State the blood parasite species.
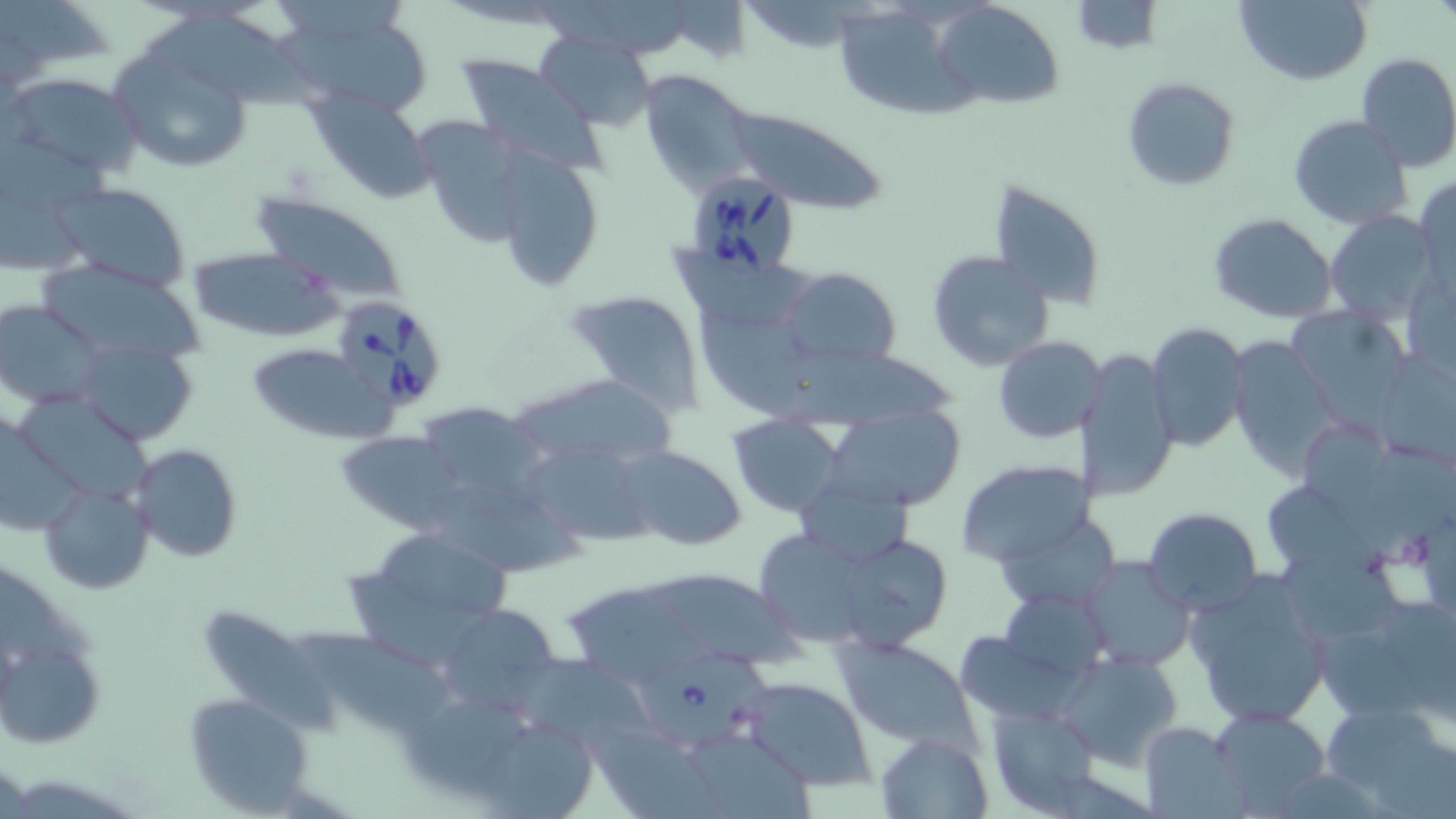
Babesia divergens.

Summary:
  - Coordinate format: approximate bounding boxes as [x1, y1, x2, y2] in pixels
  - Babesia divergens-infected red blood cell locations: [674, 169, 802, 288], [330, 294, 448, 412], [639, 649, 776, 752]
  - Uninfected red blood cell locations: [668, 0, 752, 62], [1069, 0, 1163, 53], [1235, 0, 1371, 86], [0, 2, 116, 88], [936, 2, 1061, 108], [277, 6, 430, 118], [144, 12, 326, 111], [827, 15, 990, 126], [536, 33, 655, 127], [106, 41, 256, 175], [1355, 51, 1456, 171], [455, 56, 605, 171], [641, 70, 762, 198], [6, 71, 146, 178], [1122, 76, 1241, 192], [310, 94, 436, 202], [715, 104, 886, 216], [1287, 114, 1413, 231], [418, 119, 532, 250], [494, 151, 606, 293], [1415, 176, 1456, 296], [986, 179, 1106, 310], [52, 181, 194, 292], [252, 194, 410, 304], [1326, 211, 1441, 325], [1209, 214, 1339, 324], [188, 247, 342, 342], [926, 250, 1054, 371], [672, 253, 835, 329], [37, 259, 205, 366], [779, 267, 901, 370], [565, 290, 705, 410], [0, 300, 105, 407], [1288, 309, 1412, 422], [1144, 323, 1249, 451], [994, 336, 1102, 442], [1228, 337, 1340, 476], [77, 339, 198, 446], [242, 342, 392, 445], [1076, 347, 1179, 503], [766, 348, 965, 429], [515, 373, 675, 472], [23, 392, 160, 504], [407, 399, 552, 509], [838, 408, 964, 509], [727, 415, 844, 518], [0, 421, 94, 540], [334, 429, 462, 533], [522, 440, 658, 545], [130, 444, 241, 563], [616, 446, 746, 551], [789, 458, 920, 561], [955, 458, 1094, 567], [38, 480, 153, 594], [418, 484, 596, 572], [1260, 488, 1390, 582], [1142, 507, 1261, 617], [995, 520, 1123, 612], [382, 530, 517, 615], [760, 536, 886, 644], [848, 543, 951, 652], [1081, 556, 1194, 672], [345, 557, 481, 662], [1185, 569, 1334, 730], [654, 574, 817, 675], [561, 579, 722, 686], [437, 603, 562, 719], [199, 609, 342, 741], [296, 628, 469, 733], [956, 634, 1087, 720], [2, 636, 104, 748], [834, 636, 980, 747], [506, 649, 657, 754], [1056, 650, 1184, 771], [740, 677, 876, 789], [182, 693, 313, 815], [411, 699, 536, 796], [1319, 700, 1454, 812], [989, 703, 1099, 814], [1209, 706, 1334, 814], [469, 715, 602, 818], [1139, 723, 1244, 815], [596, 731, 722, 813], [681, 731, 817, 819], [875, 731, 991, 816]
  - Modality: light microscopy
  - Field of view: single
  - Stain: May-Grünwald-Giemsa
  - Image size: 1456×819 pixels
  - Preparation: thin blood smear
  - Magnification: 1000x